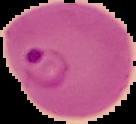
Summary:
  - Image size: 136×124 pixels
  - Image type: cell region segmented out of the field of view; surrounding area masked to black
  - Result: Plasmodium parasites identified
  - Preparation: thin blood smear